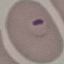

result: malaria parasites detected
capture: smartphone through the microscope eyepiece
image_type: cell patch, automatically extracted from a larger field of view and resized to 64 × 64 pixels
stain: Giemsa
preparation: thin smear